State which parasite is depicted.
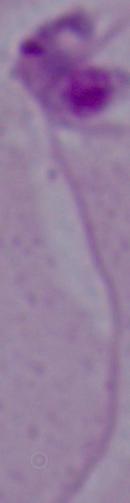
Leishmania.

Photomicrograph. 1000x magnification.